Report the malaria status of this cell.
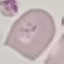
It is uninfected.

Summary:
  - Capture: smartphone camera at the microscope eyepiece
  - Image type: cell patch, automatically extracted from a larger field of view and resized to 64 × 64 pixels
  - Stain: Giemsa
  - Preparation: thin smear